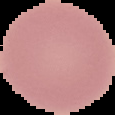
{
  "image_size": "115×115 pixels",
  "preparation": "thin blood film",
  "image_type": "segmented cell region with the area outside set to black",
  "malaria_status": "uninfected"
}